Outline each blood parasite and name the species.
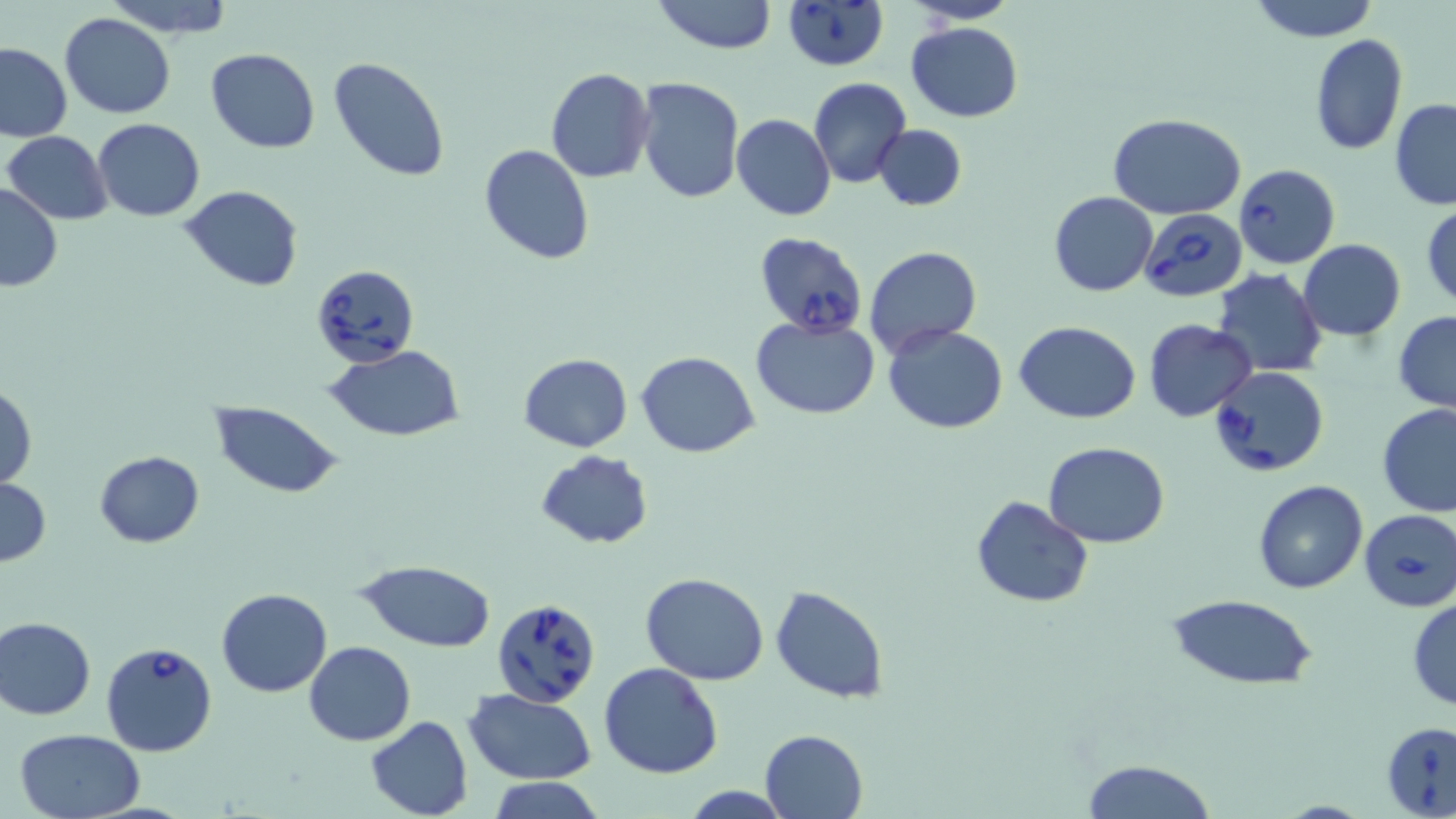
Approximate bounding boxes as (x1,y1)-(x2,y2) corner pairs in pixels.
Babesia divergens-infected red blood cells: (781,1)-(892,73), (1234,164)-(1340,269), (1140,208)-(1248,303), (753,231)-(868,333), (314,266)-(425,368), (1208,365)-(1330,477), (1358,508)-(1456,613), (492,598)-(600,709), (100,640)-(218,756), (1381,721)-(1456,818).
No Plasmodium falciparum, Plasmodium ovale, Plasmodium malariae, Plasmodium vivax, or Trypanosoma brucei observed.

Uninfected red blood cell locations: (103,0)-(235,38), (654,0)-(776,54), (905,0)-(1021,24), (1246,0)-(1380,42), (60,14)-(175,119), (906,21)-(1024,121), (1309,33)-(1407,156), (0,43)-(74,143), (206,47)-(320,152), (328,57)-(451,181), (545,67)-(655,183), (636,76)-(743,205), (808,76)-(912,189), (1390,98)-(1456,210), (731,113)-(836,221), (1109,114)-(1245,220), (93,118)-(205,220), (872,124)-(967,210), (2,131)-(113,225), (479,144)-(596,265), (0,180)-(62,294), (178,185)-(305,292), (1049,192)-(1158,296), (1422,204)-(1455,310), (1298,240)-(1406,341), (863,246)-(981,357), (1213,268)-(1326,378), (1393,311)-(1456,413), (751,314)-(879,419), (1143,318)-(1259,421), (1013,321)-(1140,424), (882,323)-(1009,433), (323,344)-(466,440), (638,352)-(759,457), (519,353)-(632,453), (0,384)-(37,488), (209,402)-(343,498), (1377,402)-(1456,517), (1043,441)-(1169,548), (95,449)-(204,546), (534,451)-(655,549), (0,478)-(50,567), (1253,479)-(1368,595), (970,495)-(1093,607), (356,560)-(498,650), (640,572)-(769,685), (770,585)-(890,702), (215,588)-(335,696), (1165,592)-(1320,691), (1407,596)-(1456,710), (0,616)-(97,721), (304,640)-(414,746), (599,663)-(723,779), (464,688)-(595,784), (365,716)-(474,819), (11,727)-(146,818), (760,729)-(868,818), (1078,758)-(1218,819), (486,778)-(606,818). Slide-level diagnosis: Babesia divergens. May-Grünwald-Giemsa-stained preparation. Light microscopy. 1000x magnification. One field of a larger specimen. Thin blood film. Image is 1456×819 pixels.